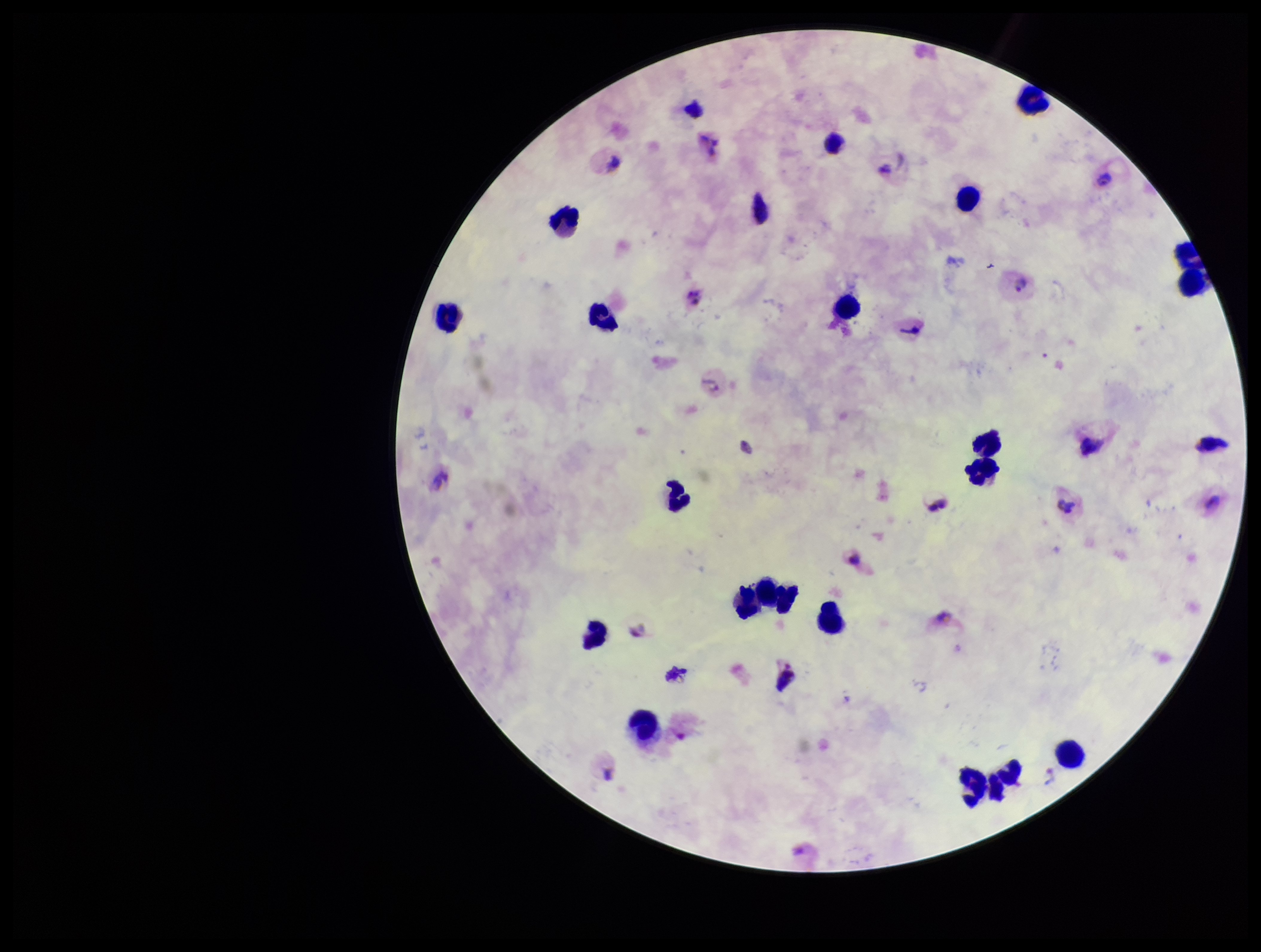
capture = smartphone photograph through the microscope eyepiece
Plasmodium parasites = detected
parasite count = 6
leukocyte count = 20
field of view = one from this slide
preparation = thick
stain = Giemsa
patient malaria status = infected
image size = 1261×952 pixels
species reported for this patient = Plasmodium vivax